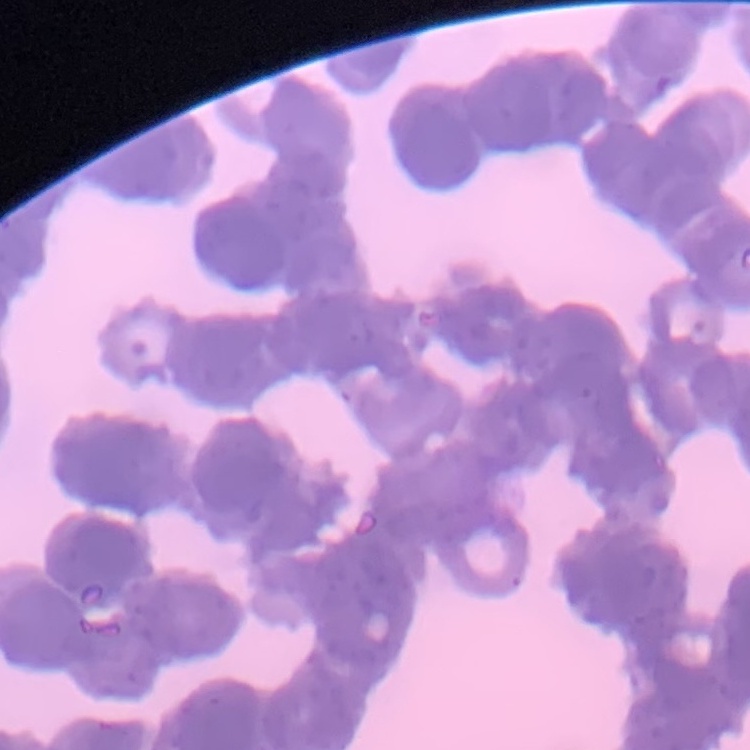

The red blood cells exhibit rouleaux formation. One tile cut from a larger photomicrograph. Thin blood smear. Stained with either Field's or Giemsa.